Locate and identify every blood parasite.
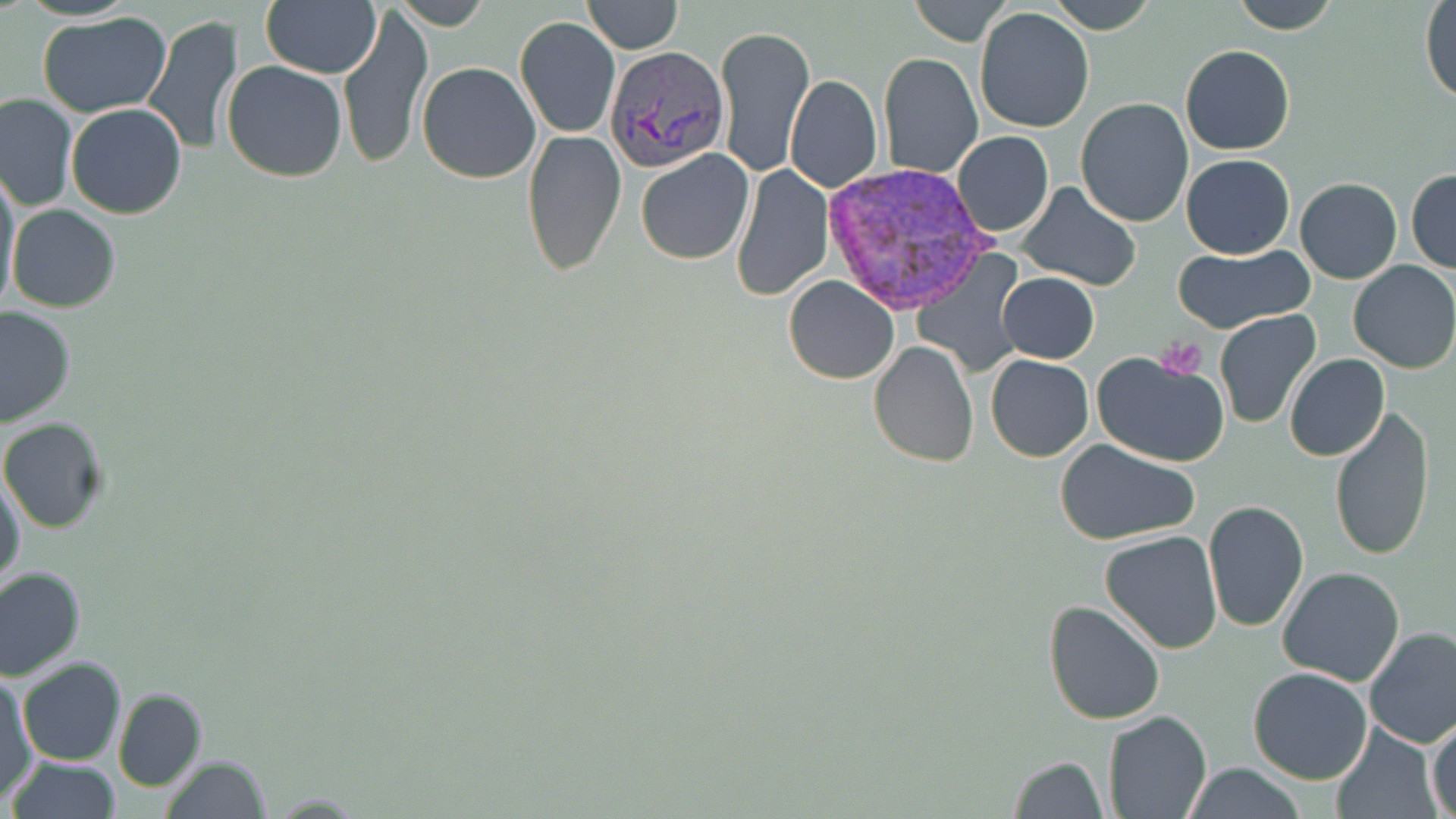

Approximate bounding boxes as [x1, y1, x2, y2] in pixels.
Plasmodium vivax-infected red blood cells: [605, 44, 733, 174], [815, 165, 1002, 316].
No Plasmodium falciparum, Plasmodium ovale, Plasmodium malariae, Babesia divergens, or Trypanosoma brucei observed.

Summary:
  - Uninfected red blood cell locations: [260, 0, 381, 79], [391, 0, 491, 30], [582, 0, 683, 53], [909, 0, 1012, 46], [1046, 0, 1157, 34], [1231, 0, 1339, 34], [1420, 2, 1455, 103], [337, 3, 433, 171], [975, 7, 1094, 134], [37, 11, 175, 118], [141, 14, 244, 156], [515, 17, 620, 139], [713, 21, 816, 180], [1179, 44, 1295, 156], [878, 53, 982, 178], [222, 61, 348, 184], [417, 63, 541, 184], [785, 76, 882, 193], [0, 92, 77, 212], [1075, 97, 1194, 227], [65, 103, 188, 219], [520, 130, 628, 276], [952, 131, 1054, 238], [634, 148, 755, 265], [1182, 153, 1295, 258], [732, 164, 833, 300], [1, 165, 21, 309], [1406, 167, 1456, 274], [1295, 177, 1402, 284], [1016, 183, 1141, 291], [7, 204, 121, 313], [1171, 243, 1314, 333], [914, 253, 1024, 374], [1348, 259, 1456, 375], [998, 271, 1100, 363], [784, 275, 899, 385], [0, 305, 75, 428], [1215, 310, 1320, 429], [868, 341, 978, 467], [1090, 350, 1232, 466], [985, 353, 1095, 462], [1285, 354, 1389, 462], [1327, 405, 1438, 563], [1, 417, 110, 534], [1055, 439, 1203, 547], [1, 471, 26, 597], [1203, 500, 1310, 634], [1098, 530, 1223, 655], [1276, 564, 1405, 686], [0, 567, 85, 679], [1042, 597, 1166, 725], [1363, 627, 1456, 748], [17, 658, 126, 767], [1248, 667, 1373, 784], [1, 676, 37, 803], [113, 688, 208, 792], [1103, 709, 1212, 819], [1427, 716, 1456, 818], [1328, 725, 1442, 819], [160, 755, 271, 819], [1009, 755, 1108, 819], [5, 756, 122, 818], [1180, 764, 1308, 819], [267, 793, 365, 816]
  - Platelet locations: [1156, 338, 1210, 379]
  - Slide-level diagnosis: Plasmodium vivax
  - Preparation: thin blood smear
  - Field of view: single
  - Stain: May-Grünwald-Giemsa
  - Magnification: 1000x
  - Modality: optical microscopy
  - Image size: 1456×819 pixels